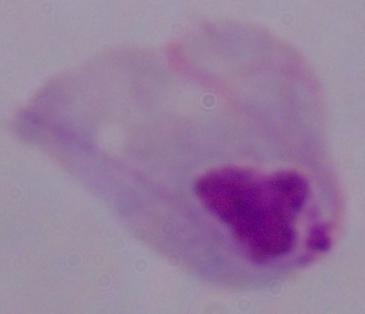

{
  "magnification": "1000x",
  "modality": "micrograph",
  "identification": "trichomonad"
}